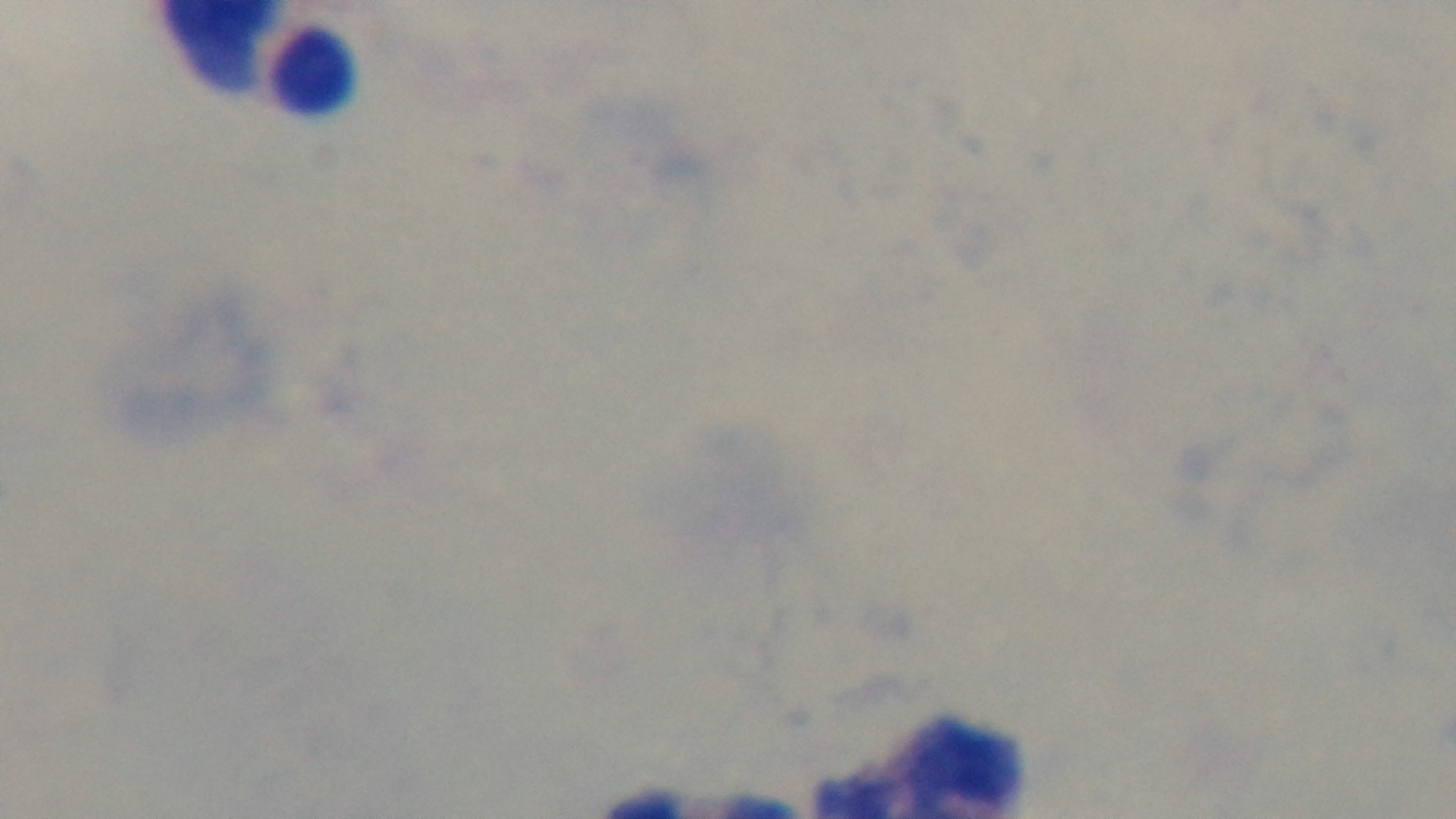 One field from the slide. Malaria status: negative. Preparation: thick smear. Oil-immersion objective, 100x. Giemsa stain. Mounted 4K digital camera. Photomicrograph.